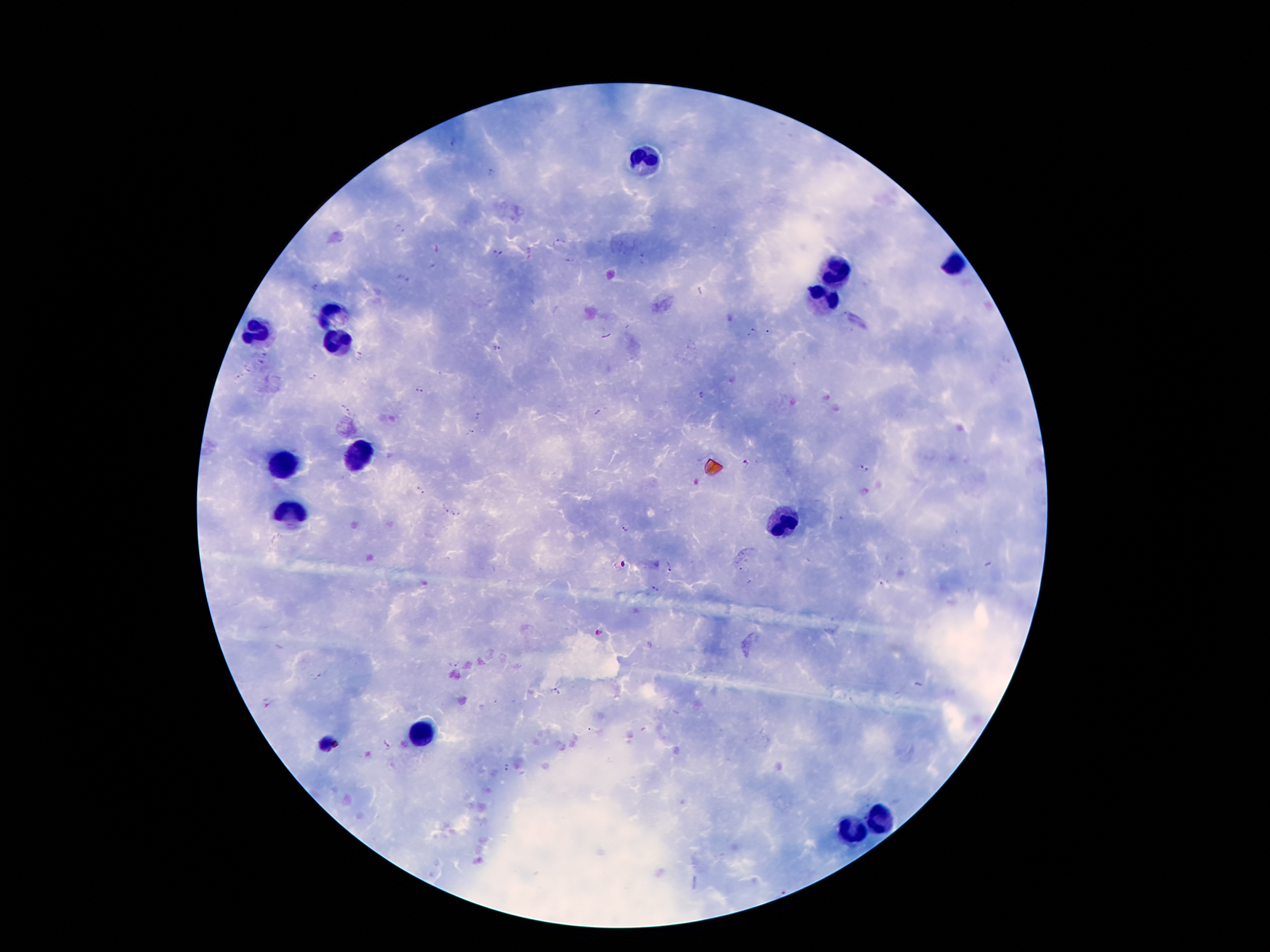
Approximate centers as {x, y} in pixels.
Summary:
  - Leukocyte locations: {646, 163}, {954, 259}, {831, 273}, {824, 301}, {336, 315}, {252, 334}, {338, 338}, {357, 457}, {285, 464}, {292, 513}, {784, 518}, {422, 732}, {880, 819}, {854, 830}
  - Plasmodium parasite locations: {453, 142}, {490, 172}, {401, 227}, {559, 241}, {497, 253}, {568, 261}, {434, 266}, {404, 279}, {314, 289}, {752, 330}, {767, 332}, {500, 350}, {266, 354}, {359, 356}, {260, 361}, {247, 368}, {238, 376}, {314, 378}, {418, 389}, {701, 395}, {346, 410}, {597, 412}, {478, 416}, {471, 432}, {746, 463}, {864, 469}, {420, 490}, {443, 509}, {457, 514}, {623, 528}, {667, 564}, {882, 581}, {654, 589}, {600, 632}, {454, 662}, {318, 677}, {554, 691}, {385, 742}, {505, 767}, {778, 891}
  - Stain: Giemsa
  - Patient malaria status: infected with Plasmodium falciparum
  - Image size: 1270×952 pixels
  - Capture: smartphone camera through the microscope eyepiece
  - Preparation: thick blood film
  - Field of view: one from this slide
  - Magnification: 100x